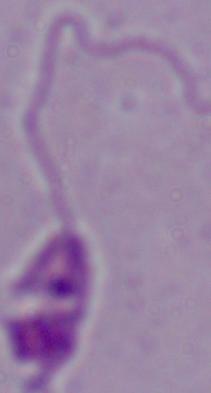

{
  "magnification": "1000x",
  "modality": "photomicrograph",
  "identification": "Leishmania"
}